Classify this cell by malaria status.
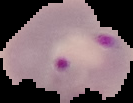

Parasitized.

Segmented cell region on a black background. From a thin blood film. Image is 133×103 pixels.